Classify this cell by malaria status.
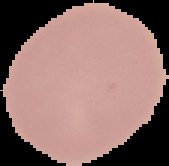
Uninfected.

Summary:
  - Preparation: thin blood smear
  - Image size: 169×166 pixels
  - Image type: segmented cell region with the area outside set to black